Comment on the morphology of the erythrocytes.
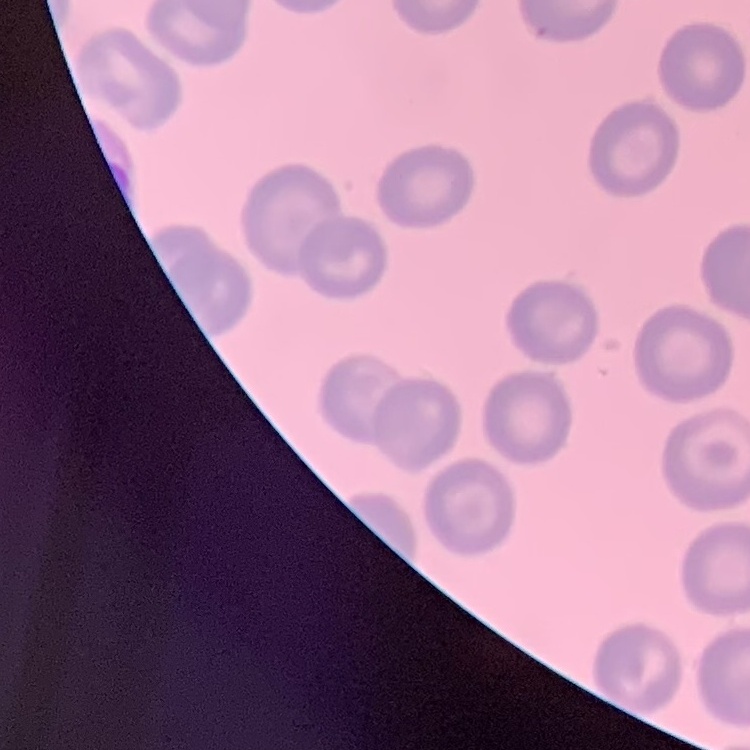
No rouleaux formation.

image type = one tile cut from a larger photomicrograph
stain = Field's or Giemsa
preparation = thin blood smear